Assess this cell for malaria.
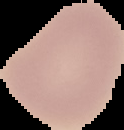
Uninfected.

{
  "image_type": "cell region segmented out of the field of view; surrounding area masked to black",
  "preparation": "thin blood smear",
  "image_size": "124×130 pixels"
}